Give the position of every malaria parasite and every leukocyte.
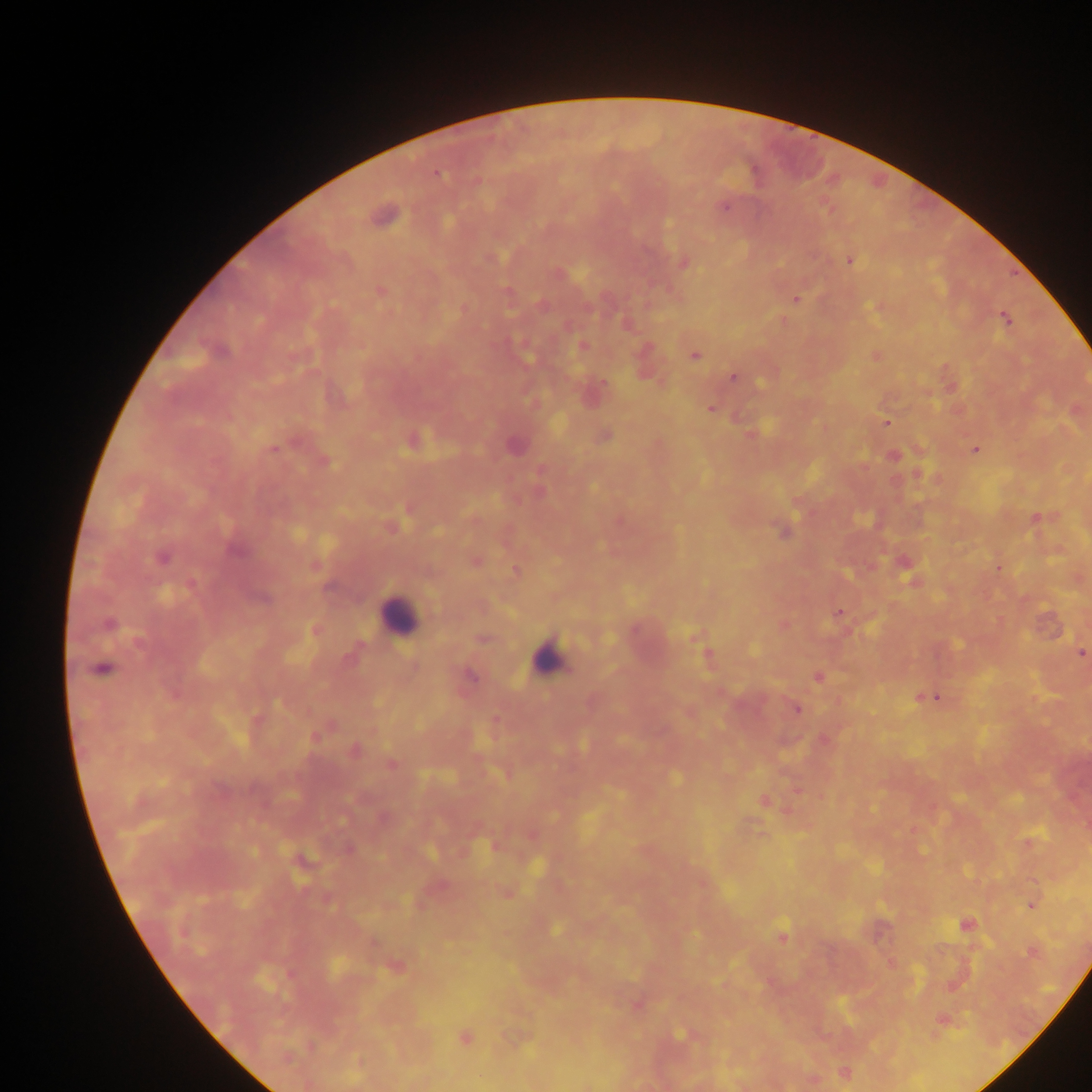

Approximate centers as x y in pixels.
Malaria parasites: 437 173; 724 207; 383 216; 492 258; 850 261; 684 265; 379 291; 796 300; 1005 319; 626 325; 582 347; 694 355; 733 378; 603 384; 711 410; 886 422; 605 436; 514 446; 273 449; 976 450; 326 462; 1036 518; 784 532; 236 550; 162 558; 999 568; 514 570; 262 600; 838 613; 109 624; 139 641; 1082 654; 707 655; 103 669; 470 676; 818 676; 933 697; 797 710; 315 738; 354 750; 392 764; 765 800; 1032 906; 966 925; 555 930; 782 935; 1032 952; 681 1034; 465 1038; 845 1074.
Leukocytes: 398 614; 550 655.

Summary:
  - Image size: 1092×1092 pixels
  - Capture: mobile-phone photograph through a microscope
  - Country: Ghana
  - Preparation: thick blood film
  - Field of view: single